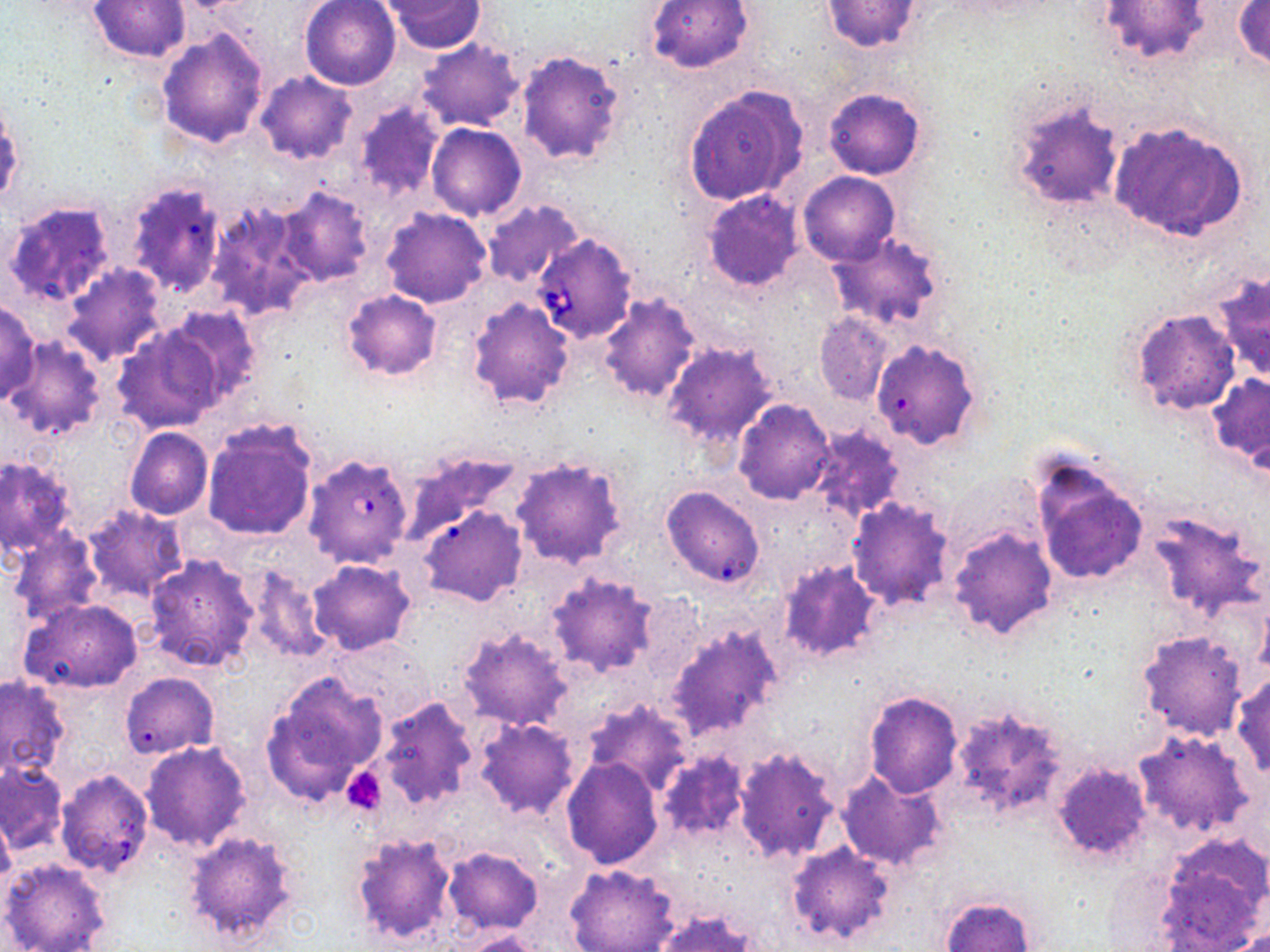

Summary:
  - Coordinate format: approximate bounding boxes as (x1, y1, x2, y2) in pixels
  - Babesia divergens-infected red blood cell locations: (532, 233, 638, 343), (304, 458, 409, 570)
  - Platelet locations: (343, 766, 386, 816)
  - Uninfected red blood cell locations: (89, 0, 190, 63), (301, 0, 401, 88), (383, 0, 489, 52), (646, 0, 753, 74), (1096, 0, 1213, 69), (820, 1, 923, 52), (1233, 2, 1270, 72), (156, 27, 269, 148), (415, 37, 524, 132), (515, 48, 627, 165), (255, 71, 358, 164), (684, 84, 808, 205), (824, 87, 925, 180), (1006, 93, 1126, 214), (352, 103, 445, 202), (1109, 119, 1250, 241), (425, 123, 527, 221), (799, 171, 899, 266), (126, 182, 226, 298), (276, 185, 376, 285), (702, 190, 806, 294), (4, 200, 116, 309), (208, 200, 315, 319), (482, 200, 585, 290), (380, 207, 491, 309), (827, 230, 948, 333), (63, 263, 169, 364), (1210, 270, 1270, 386), (342, 290, 443, 380), (465, 297, 576, 411), (596, 297, 700, 407), (0, 301, 41, 404), (165, 305, 263, 403), (1125, 306, 1241, 417), (813, 313, 894, 406), (111, 322, 225, 435), (5, 337, 109, 441), (870, 337, 981, 450), (661, 339, 780, 450), (1206, 374, 1270, 469), (733, 399, 837, 504), (201, 420, 318, 540), (808, 426, 906, 522), (124, 427, 212, 519), (403, 446, 526, 543), (0, 456, 77, 558), (510, 456, 630, 570), (1029, 456, 1150, 590), (660, 486, 765, 589), (845, 498, 955, 609), (83, 505, 187, 599), (417, 505, 527, 606), (1142, 508, 1267, 629), (946, 524, 1058, 642), (9, 529, 104, 625), (144, 553, 261, 673), (305, 558, 417, 655), (775, 560, 885, 666), (244, 564, 330, 664), (546, 574, 658, 679), (633, 590, 704, 688), (19, 598, 144, 694), (664, 621, 783, 742), (457, 625, 574, 732), (1136, 631, 1249, 742), (330, 635, 434, 722), (120, 673, 219, 759), (261, 673, 387, 806), (1231, 673, 1270, 780), (0, 676, 70, 781), (864, 689, 963, 798), (372, 697, 481, 811), (581, 697, 692, 795), (950, 703, 1072, 824), (474, 718, 581, 820), (1133, 731, 1255, 837), (140, 740, 252, 852), (732, 745, 841, 864), (656, 749, 751, 842), (560, 758, 664, 869), (1051, 762, 1151, 868), (0, 763, 69, 855), (835, 767, 948, 872), (54, 768, 155, 877), (0, 810, 16, 892), (182, 829, 303, 948), (349, 830, 459, 948), (785, 841, 896, 948), (1155, 841, 1268, 949), (441, 844, 543, 934), (0, 857, 112, 952), (565, 862, 680, 952), (938, 894, 1037, 952), (649, 909, 762, 952), (454, 929, 550, 951)
  - Slide-level diagnosis: Babesia divergens
  - Modality: optical microscopy
  - Image size: 1270×952 pixels
  - Stain: May-Grünwald-Giemsa
  - Preparation: thin blood film
  - Field of view: one of a larger specimen
  - Magnification: 1000x